Identify the cell.
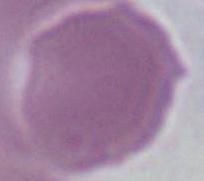
An erythrocyte.

{
  "magnification": "1000x",
  "modality": "photomicrograph"
}